Identify the blood parasite species.
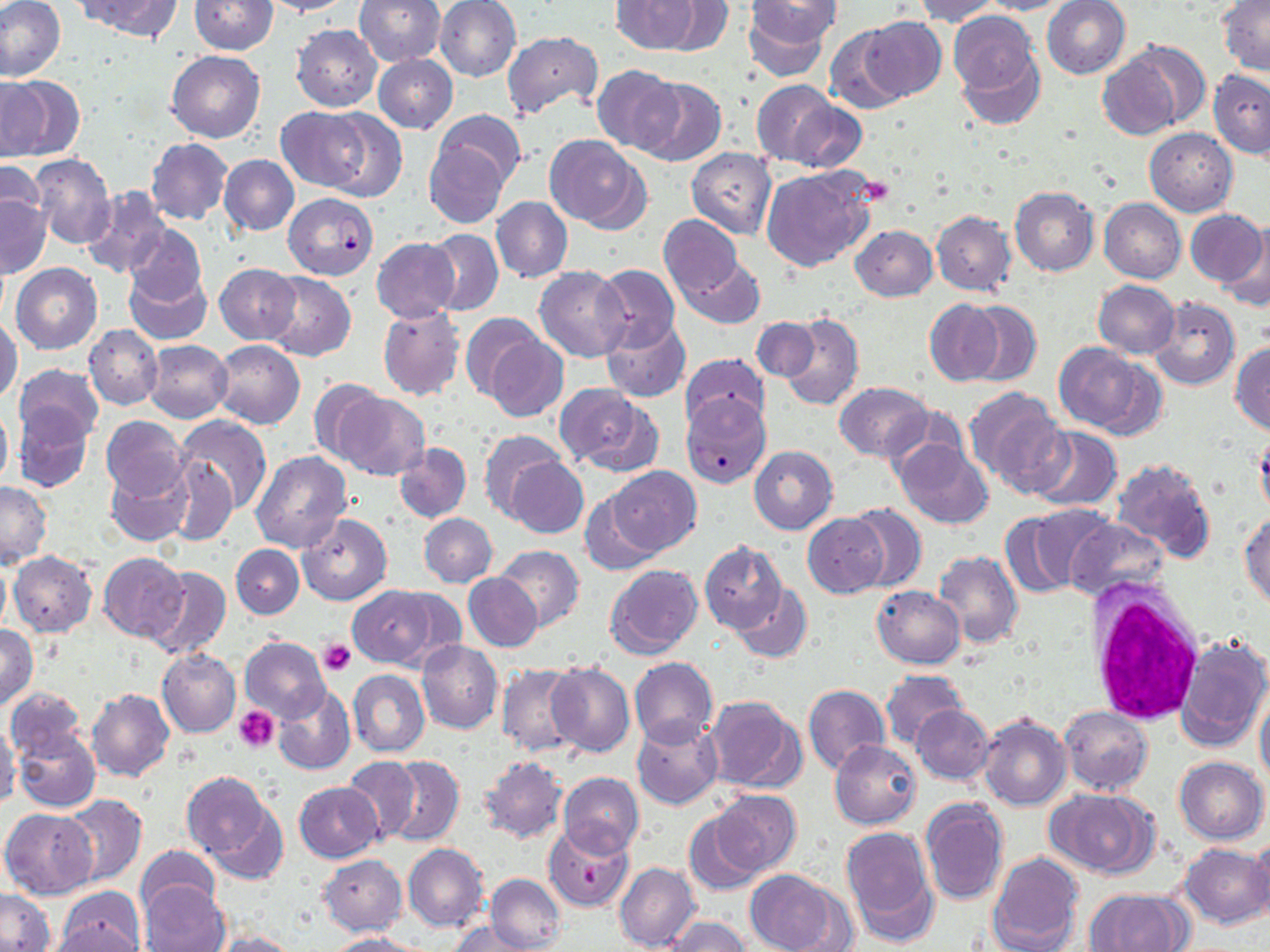

Plasmodium falciparum.

Summary:
  - Coordinate format: approximate bounding boxes as named x1/y1/x2/y2 corners in pixels
  - White blood cell locations: (x1=1087, y1=585, x2=1206, y2=728)
  - Platelet locations: (x1=858, y1=176, x2=895, y2=207), (x1=318, y1=639, x2=355, y2=677), (x1=235, y1=706, x2=280, y2=751), (x1=579, y1=865, x2=603, y2=888)
  - Uninfected red blood cell locations: (x1=0, y1=0, x2=67, y2=83), (x1=80, y1=0, x2=182, y2=42), (x1=190, y1=0, x2=277, y2=54), (x1=260, y1=0, x2=353, y2=16), (x1=354, y1=0, x2=445, y2=66), (x1=435, y1=0, x2=521, y2=82), (x1=613, y1=0, x2=699, y2=54), (x1=657, y1=0, x2=733, y2=55), (x1=743, y1=0, x2=835, y2=80), (x1=912, y1=0, x2=1001, y2=24), (x1=979, y1=0, x2=1070, y2=15), (x1=1042, y1=0, x2=1131, y2=79), (x1=1219, y1=0, x2=1270, y2=75), (x1=947, y1=10, x2=1039, y2=97), (x1=860, y1=17, x2=945, y2=101), (x1=291, y1=25, x2=382, y2=111), (x1=825, y1=26, x2=909, y2=114), (x1=294, y1=30, x2=387, y2=198), (x1=501, y1=31, x2=602, y2=119), (x1=1115, y1=39, x2=1211, y2=135), (x1=168, y1=50, x2=265, y2=144), (x1=957, y1=50, x2=1044, y2=133), (x1=372, y1=54, x2=457, y2=133), (x1=1095, y1=60, x2=1177, y2=141), (x1=593, y1=64, x2=680, y2=154), (x1=1209, y1=71, x2=1270, y2=158), (x1=1, y1=73, x2=81, y2=161), (x1=634, y1=78, x2=726, y2=166), (x1=750, y1=79, x2=845, y2=169), (x1=785, y1=99, x2=868, y2=174), (x1=314, y1=107, x2=407, y2=202), (x1=277, y1=108, x2=368, y2=191), (x1=433, y1=109, x2=525, y2=188), (x1=1145, y1=128, x2=1237, y2=216), (x1=544, y1=135, x2=650, y2=231), (x1=145, y1=137, x2=231, y2=225), (x1=423, y1=140, x2=511, y2=229), (x1=687, y1=147, x2=776, y2=240), (x1=29, y1=154, x2=115, y2=249), (x1=219, y1=155, x2=299, y2=236), (x1=0, y1=162, x2=45, y2=237), (x1=761, y1=165, x2=877, y2=272), (x1=82, y1=186, x2=172, y2=280), (x1=1010, y1=186, x2=1099, y2=276), (x1=0, y1=194, x2=51, y2=279), (x1=491, y1=196, x2=572, y2=283), (x1=1099, y1=199, x2=1185, y2=283), (x1=1186, y1=209, x2=1267, y2=288), (x1=931, y1=210, x2=1016, y2=297), (x1=659, y1=214, x2=742, y2=299), (x1=1222, y1=222, x2=1270, y2=314), (x1=123, y1=223, x2=207, y2=307), (x1=850, y1=225, x2=938, y2=301), (x1=425, y1=229, x2=502, y2=316), (x1=371, y1=237, x2=461, y2=323), (x1=680, y1=256, x2=765, y2=328), (x1=11, y1=263, x2=102, y2=353), (x1=592, y1=263, x2=680, y2=352), (x1=214, y1=264, x2=301, y2=343), (x1=535, y1=266, x2=631, y2=362), (x1=124, y1=268, x2=211, y2=344), (x1=264, y1=271, x2=356, y2=361), (x1=1093, y1=281, x2=1180, y2=358), (x1=1150, y1=296, x2=1240, y2=392), (x1=925, y1=300, x2=1003, y2=385), (x1=965, y1=302, x2=1041, y2=387), (x1=377, y1=307, x2=465, y2=401), (x1=777, y1=311, x2=865, y2=413), (x1=461, y1=313, x2=545, y2=402), (x1=601, y1=316, x2=690, y2=403), (x1=0, y1=317, x2=22, y2=406), (x1=751, y1=317, x2=823, y2=383), (x1=85, y1=325, x2=162, y2=409), (x1=486, y1=335, x2=568, y2=422), (x1=212, y1=339, x2=304, y2=429), (x1=143, y1=340, x2=233, y2=422), (x1=1053, y1=342, x2=1154, y2=434), (x1=1231, y1=342, x2=1270, y2=436), (x1=678, y1=354, x2=770, y2=434), (x1=13, y1=364, x2=104, y2=445), (x1=309, y1=378, x2=388, y2=462), (x1=835, y1=382, x2=933, y2=461), (x1=553, y1=383, x2=657, y2=474), (x1=962, y1=386, x2=1068, y2=494), (x1=333, y1=391, x2=429, y2=480), (x1=0, y1=405, x2=13, y2=489), (x1=14, y1=405, x2=93, y2=492), (x1=101, y1=416, x2=189, y2=500), (x1=175, y1=416, x2=272, y2=513), (x1=1026, y1=426, x2=1122, y2=511), (x1=479, y1=430, x2=563, y2=521), (x1=1256, y1=431, x2=1270, y2=522), (x1=893, y1=437, x2=993, y2=528), (x1=393, y1=443, x2=470, y2=522), (x1=749, y1=446, x2=837, y2=534), (x1=250, y1=451, x2=352, y2=554), (x1=164, y1=457, x2=236, y2=544), (x1=505, y1=457, x2=588, y2=538), (x1=1111, y1=458, x2=1217, y2=561), (x1=107, y1=460, x2=193, y2=548), (x1=609, y1=466, x2=699, y2=556), (x1=1, y1=479, x2=51, y2=567), (x1=580, y1=489, x2=665, y2=575), (x1=846, y1=503, x2=927, y2=591), (x1=1006, y1=505, x2=1110, y2=596), (x1=1240, y1=512, x2=1270, y2=609), (x1=419, y1=513, x2=498, y2=587), (x1=803, y1=513, x2=888, y2=596), (x1=298, y1=515, x2=392, y2=606), (x1=1065, y1=517, x2=1169, y2=603), (x1=700, y1=541, x2=787, y2=634), (x1=231, y1=544, x2=304, y2=619), (x1=494, y1=544, x2=585, y2=631), (x1=932, y1=550, x2=1022, y2=648), (x1=8, y1=551, x2=97, y2=636), (x1=98, y1=552, x2=190, y2=642), (x1=0, y1=559, x2=11, y2=636), (x1=604, y1=564, x2=704, y2=660), (x1=143, y1=566, x2=231, y2=661), (x1=464, y1=573, x2=543, y2=650), (x1=733, y1=583, x2=813, y2=662), (x1=349, y1=585, x2=441, y2=668), (x1=871, y1=586, x2=964, y2=668), (x1=0, y1=625, x2=39, y2=710), (x1=1176, y1=633, x2=1270, y2=752), (x1=241, y1=637, x2=330, y2=723), (x1=417, y1=640, x2=503, y2=734), (x1=157, y1=649, x2=240, y2=737), (x1=629, y1=657, x2=717, y2=747), (x1=546, y1=661, x2=635, y2=757), (x1=496, y1=662, x2=582, y2=758), (x1=348, y1=669, x2=430, y2=757), (x1=881, y1=669, x2=968, y2=750), (x1=273, y1=685, x2=356, y2=777), (x1=803, y1=685, x2=890, y2=775), (x1=5, y1=686, x2=87, y2=761), (x1=87, y1=688, x2=174, y2=781), (x1=1255, y1=691, x2=1270, y2=789), (x1=702, y1=695, x2=807, y2=792), (x1=911, y1=705, x2=994, y2=784), (x1=1059, y1=706, x2=1153, y2=796), (x1=978, y1=714, x2=1070, y2=811), (x1=632, y1=719, x2=723, y2=812), (x1=0, y1=722, x2=22, y2=807), (x1=14, y1=730, x2=100, y2=812), (x1=830, y1=739, x2=922, y2=830), (x1=343, y1=755, x2=421, y2=844), (x1=384, y1=755, x2=464, y2=846), (x1=477, y1=756, x2=567, y2=842), (x1=1173, y1=756, x2=1267, y2=844), (x1=181, y1=771, x2=276, y2=866), (x1=558, y1=772, x2=643, y2=856), (x1=295, y1=781, x2=383, y2=863), (x1=1046, y1=788, x2=1159, y2=877), (x1=707, y1=789, x2=801, y2=875), (x1=61, y1=794, x2=146, y2=886), (x1=920, y1=798, x2=1008, y2=907), (x1=202, y1=804, x2=287, y2=887), (x1=1, y1=808, x2=98, y2=898), (x1=683, y1=811, x2=768, y2=897), (x1=543, y1=823, x2=636, y2=913), (x1=840, y1=825, x2=938, y2=943), (x1=1250, y1=834, x2=1270, y2=922), (x1=402, y1=844, x2=489, y2=932), (x1=1179, y1=844, x2=1269, y2=928), (x1=137, y1=847, x2=221, y2=917), (x1=987, y1=851, x2=1084, y2=952), (x1=318, y1=854, x2=407, y2=935), (x1=614, y1=862, x2=699, y2=952), (x1=748, y1=871, x2=847, y2=952), (x1=486, y1=873, x2=565, y2=951), (x1=140, y1=879, x2=229, y2=952), (x1=54, y1=887, x2=144, y2=951), (x1=0, y1=888, x2=54, y2=951), (x1=1083, y1=889, x2=1189, y2=952), (x1=662, y1=916, x2=750, y2=952), (x1=44, y1=922, x2=142, y2=952), (x1=448, y1=922, x2=534, y2=951), (x1=209, y1=931, x2=302, y2=952), (x1=324, y1=933, x2=427, y2=952)
  - Plasmodium falciparum-infected red blood cell locations: (x1=283, y1=192, x2=378, y2=280), (x1=681, y1=393, x2=772, y2=490)
  - Field of view: single
  - Modality: optical microscopy
  - Stain: May-Grünwald-Giemsa
  - Magnification: 1000x
  - Preparation: thin blood film
  - Image size: 1270×952 pixels